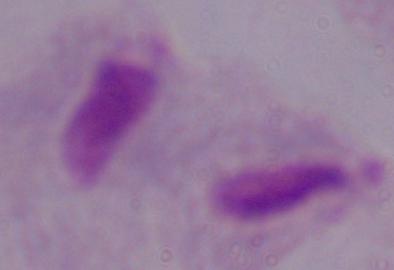 Micrograph. 1000x magnification. A trichomonad is shown.